Locate every blood parasite and identify its species.
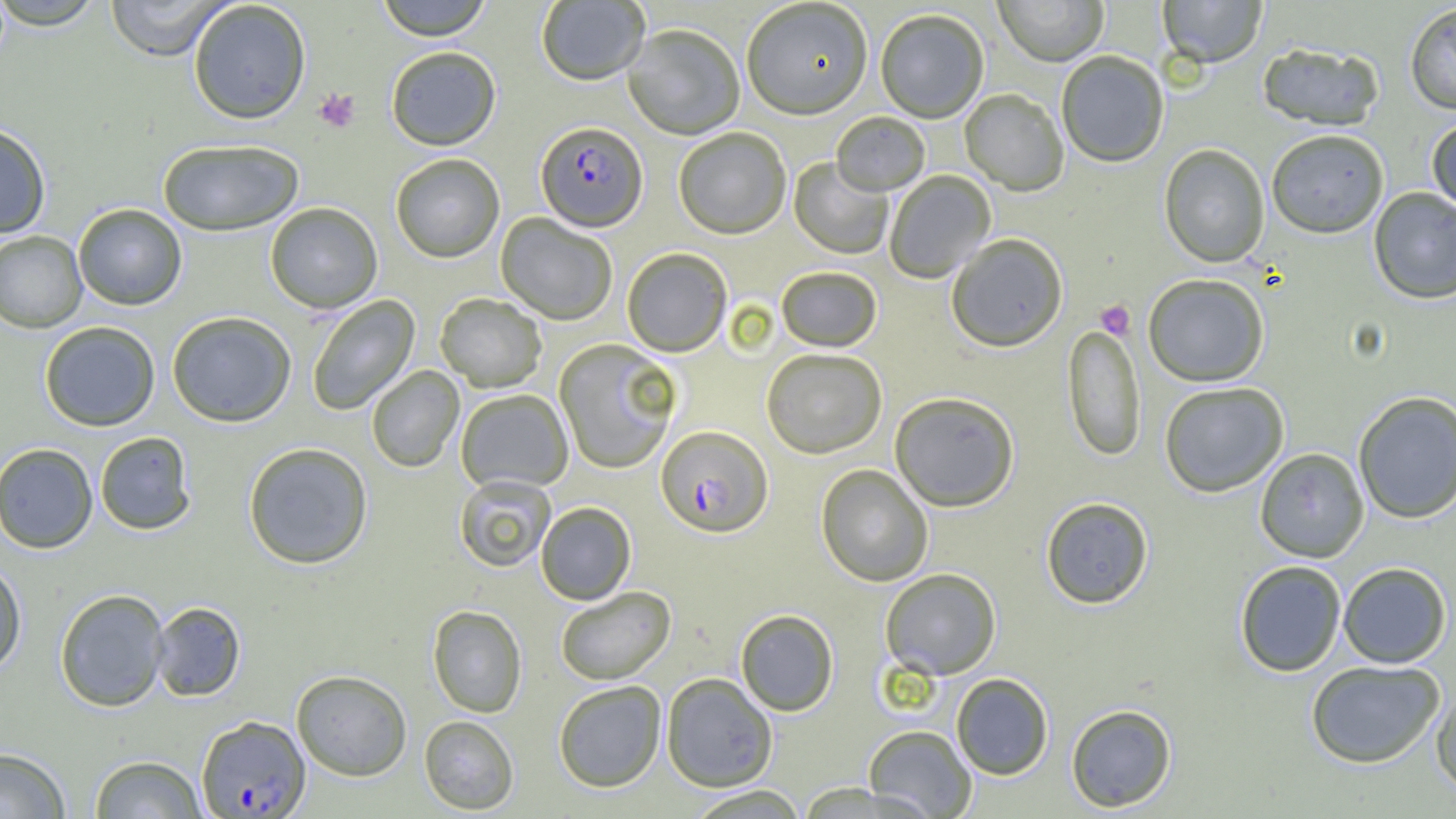
Approximate bounding boxes as (x1,y1)-(x2,y2) corner pairs in pixels.
Plasmodium falciparum-infected red blood cells: (535,122)-(648,234), (655,426)-(773,540), (196,715)-(310,818).
No Plasmodium ovale, Plasmodium malariae, Plasmodium vivax, Babesia divergens, or Trypanosoma brucei observed.

{
  "slide_level_diagnosis": "Plasmodium falciparum",
  "image_size": "1456×819 pixels",
  "field_of_view": "one of a larger specimen",
  "preparation": "thin blood smear",
  "uninfected_red_blood_cell_locations": "approximate bounding boxes as (x1,y1)-(x2,y2) corner pairs in pixels: (102,0)-(236,61), (375,0)-(493,42), (993,0)-(1109,68), (1157,0)-(1267,70), (0,1)-(109,32), (537,1)-(650,88), (187,2)-(312,126), (741,2)-(874,122), (1404,3)-(1456,116), (875,11)-(989,125), (623,26)-(744,142), (1257,43)-(1385,132), (386,48)-(501,153), (1056,53)-(1169,169), (959,90)-(1068,197), (831,113)-(930,198), (1427,117)-(1456,218), (0,122)-(52,239), (674,129)-(791,241), (1266,130)-(1389,240), (157,140)-(304,237), (1158,145)-(1269,269), (391,155)-(505,264), (789,158)-(893,260), (885,171)-(996,284), (1369,187)-(1456,305), (73,203)-(187,310), (265,203)-(383,314), (496,214)-(617,326), (0,231)-(87,333), (947,235)-(1068,354), (622,249)-(731,358), (776,267)-(882,353), (1143,275)-(1270,388), (435,294)-(547,394), (307,295)-(421,415), (166,311)-(296,428), (39,321)-(161,431), (1062,324)-(1146,464), (554,340)-(680,474), (761,350)-(887,460), (367,366)-(464,473), (1160,382)-(1289,497), (456,390)-(573,494), (1353,391)-(1456,525), (890,394)-(1019,513), (95,432)-(196,535), (243,442)-(373,570), (0,443)-(98,554), (1255,448)-(1369,563), (816,465)-(933,587), (454,476)-(556,573), (1040,497)-(1154,610), (536,502)-(636,606), (0,559)-(27,677), (1234,560)-(1347,677), (1337,562)-(1452,668), (881,569)-(1001,680), (556,586)-(676,686), (54,588)-(170,712), (150,602)-(245,701), (427,605)-(527,718), (735,609)-(839,716), (1305,660)-(1445,768), (291,669)-(412,781), (661,673)-(778,792), (951,673)-(1053,780), (553,681)-(666,793), (1431,683)-(1456,794), (1066,703)-(1177,813), (419,715)-(519,815), (863,725)-(977,818), (0,747)-(71,818), (89,754)-(207,818), (685,786)-(810,818)",
  "magnification": "1000x",
  "modality": "light microscopy",
  "platelet_locations": "approximate bounding boxes as (x1,y1)-(x2,y2) corner pairs in pixels: (313,88)-(361,132), (1095,300)-(1135,340)"
}